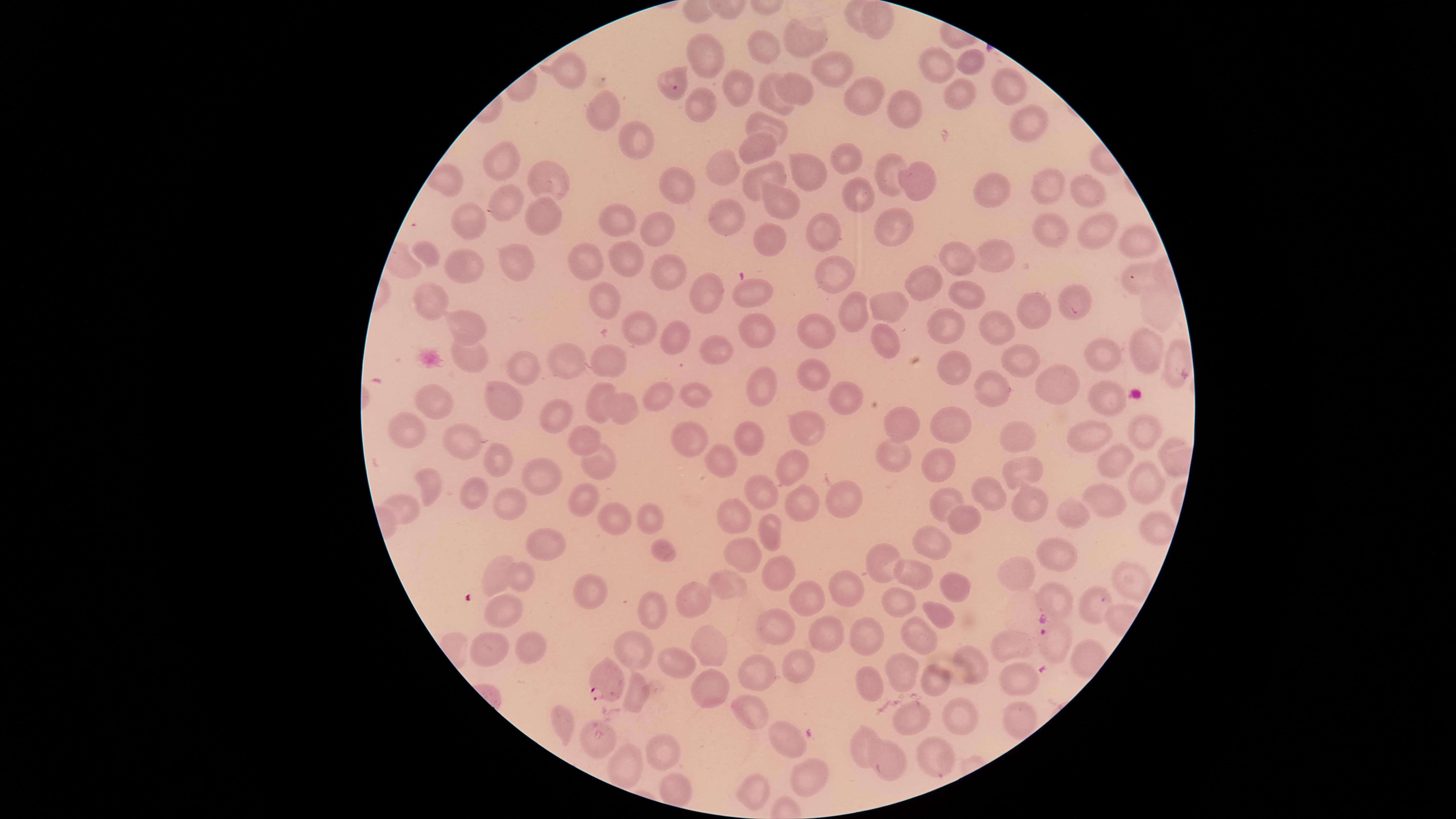
{
  "species": "Plasmodium falciparum",
  "uninfected_RBCs": "approximate marker points as [x, y] in pixels: [851, 13], [878, 23], [805, 39], [764, 53], [704, 60], [971, 64], [936, 67], [826, 70], [566, 72], [675, 72], [743, 82], [1009, 84], [797, 90], [954, 92], [866, 98], [769, 101], [700, 102], [909, 108], [606, 118], [773, 125], [1027, 125], [638, 145], [760, 146], [851, 159], [506, 163], [880, 167], [723, 169], [806, 170], [776, 175], [912, 175], [678, 180], [1046, 182], [552, 185], [994, 188], [1091, 189], [859, 202], [779, 206], [504, 208], [893, 212], [728, 214], [540, 219], [611, 221], [468, 222], [658, 226], [820, 230], [1051, 230], [1096, 231], [1135, 241], [764, 243], [428, 256], [998, 257], [952, 258], [513, 262], [583, 262], [621, 263], [463, 269], [667, 271], [837, 273], [1135, 274], [923, 281], [707, 286], [754, 288], [1077, 294], [432, 295], [969, 295], [605, 302], [894, 304], [1152, 305], [862, 307], [1036, 311], [851, 317], [467, 326], [639, 327], [943, 327], [758, 329], [997, 329], [811, 333], [887, 337], [672, 339], [1144, 346], [710, 349], [1107, 356], [1176, 356], [468, 357], [555, 361], [1014, 361], [598, 362], [509, 363], [949, 364], [815, 376], [1055, 377], [761, 385], [991, 389], [696, 390], [847, 394], [658, 396], [1104, 398], [434, 400], [498, 404], [595, 407], [624, 410], [557, 416], [407, 426], [806, 426], [898, 427], [1144, 431], [946, 432], [1093, 436], [579, 439], [1017, 439], [687, 441], [747, 443], [466, 445], [498, 455], [723, 461], [598, 462], [886, 463], [1117, 463], [791, 467], [1018, 468], [935, 469], [542, 470], [432, 485], [1148, 485], [757, 491], [471, 496], [842, 497], [940, 498], [987, 500], [578, 502], [798, 502], [1020, 502], [1111, 502], [512, 504], [410, 506], [1075, 517], [615, 518], [647, 520], [736, 520], [958, 520], [1151, 531], [768, 533], [545, 539], [931, 541], [660, 550], [1057, 558], [743, 560], [495, 563], [879, 567], [781, 576], [1025, 576], [917, 577], [1126, 581], [521, 582], [953, 584], [733, 586], [846, 587], [597, 589], [805, 594], [701, 600], [900, 600], [1065, 602], [1097, 607], [653, 612], [503, 613], [934, 615], [824, 628], [774, 632], [919, 637], [865, 639], [1010, 644], [489, 647], [531, 648], [711, 649], [637, 652], [673, 660], [797, 660], [967, 660], [759, 666], [1014, 679], [897, 681], [938, 681], [707, 686], [871, 690], [635, 692], [745, 707], [968, 714], [1014, 714], [914, 716], [560, 717], [595, 736], [787, 737], [864, 742], [656, 752], [896, 757], [930, 760], [630, 766], [807, 771], [670, 790], [749, 791]",
  "stain": "Giemsa",
  "image_size": "1456×819 pixels",
  "preparation": "thin blood smear",
  "visible_region": "circular",
  "field_of_view": "single",
  "capture": "smartphone photograph through the microscope eyepiece",
  "presence": "malaria parasites seen",
  "parasitized_RBCs": "approximate marker points as [x, y] in pixels: [1023, 614], [1052, 641], [608, 682]"
}